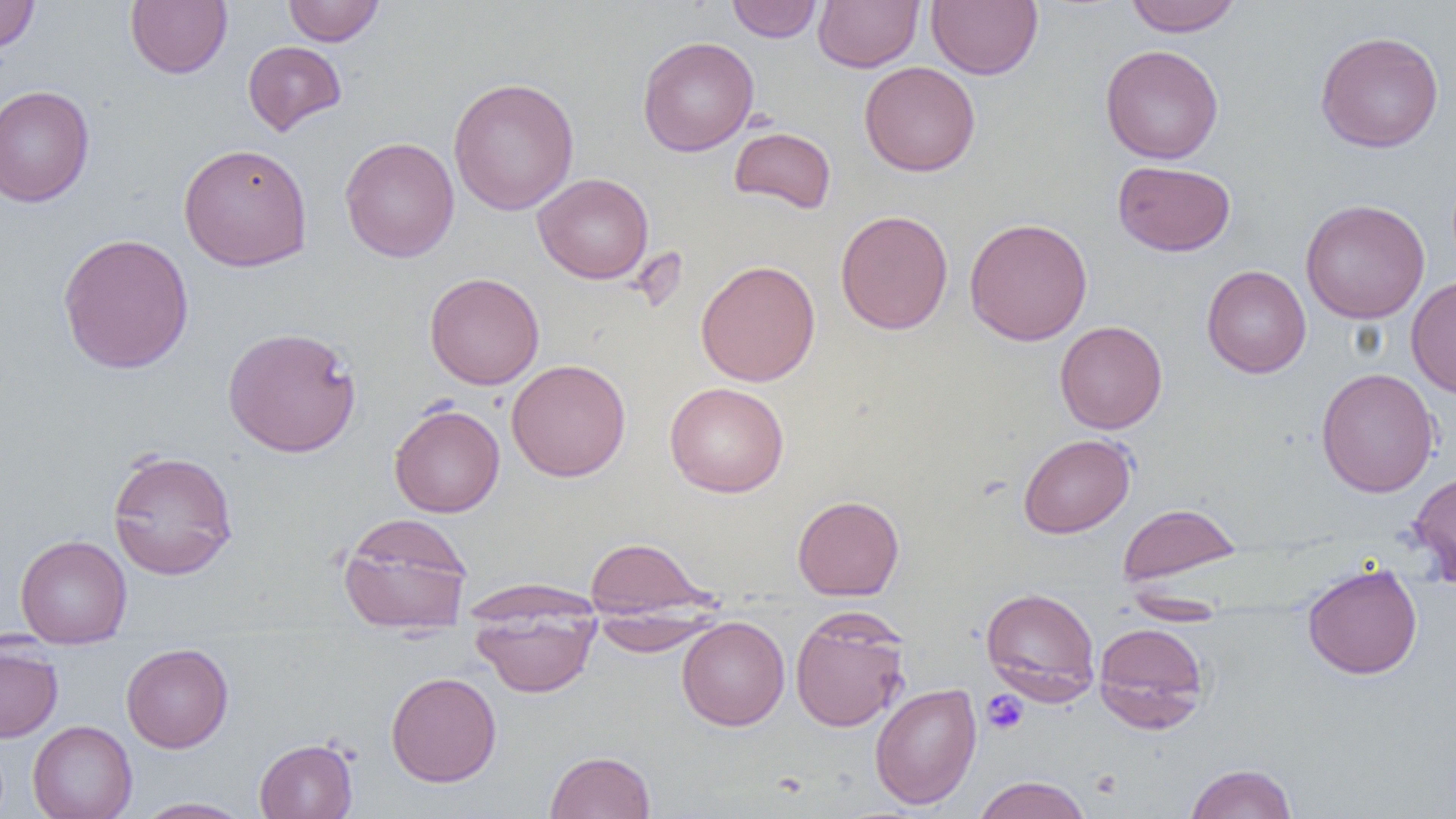 Approximate bounding boxes as (x1,y1)-(x2,y2) corner pairs in pixels. Platelet locations: (981,689)-(1029,735). Uninfected red blood cell locations: (0,0)-(39,54), (126,0)-(232,78), (283,0)-(384,46), (727,0)-(822,42), (814,0)-(923,72), (926,0)-(1042,80), (1124,0)-(1241,36), (1314,31)-(1444,153), (637,36)-(759,157), (242,41)-(347,135), (1100,44)-(1224,164), (859,61)-(980,176), (448,77)-(579,216), (0,84)-(95,207), (729,126)-(837,214), (340,137)-(459,262), (178,142)-(312,272), (1112,160)-(1235,256), (533,173)-(654,283), (1300,199)-(1430,324), (835,209)-(953,335), (964,217)-(1093,346), (57,232)-(194,374), (695,259)-(821,386), (1201,265)-(1311,377), (425,272)-(545,389), (1406,276)-(1456,398), (1054,320)-(1167,434), (222,326)-(361,457), (506,359)-(631,481), (1315,368)-(1439,497), (664,381)-(789,497), (389,403)-(505,517), (1018,433)-(1135,538), (107,448)-(239,581), (1408,471)-(1456,585), (792,495)-(904,600), (1117,502)-(1242,588), (338,512)-(473,635), (15,534)-(132,648), (584,536)-(712,619), (1302,563)-(1423,679), (465,579)-(603,623), (980,586)-(1101,702), (1123,594)-(1231,624), (470,602)-(599,697), (790,609)-(910,732), (590,612)-(723,656), (677,616)-(790,731), (1093,622)-(1210,732), (0,640)-(63,742), (121,643)-(234,752), (386,671)-(502,787), (869,683)-(982,810), (27,720)-(137,819), (254,739)-(358,818), (545,750)-(656,819), (1184,763)-(1297,819), (971,775)-(1092,819), (134,797)-(252,818). Slide-level diagnosis: no evidence of blood parasites. Image is 1456×819 pixels. Thin blood film. Single field of view. Captured at 1000x magnification. Optical microscopy.